Outline each blood parasite and name the species.
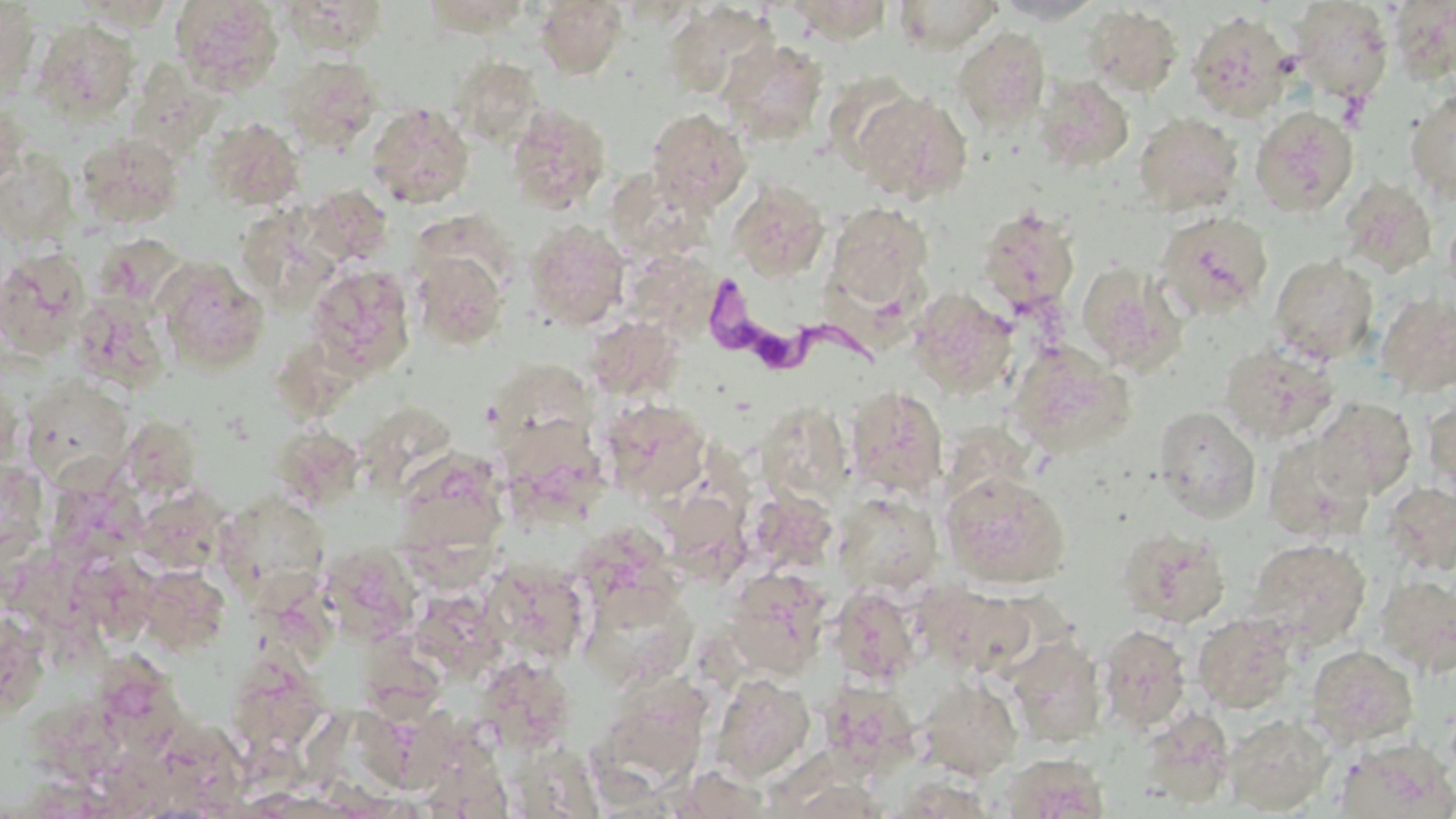
Approximate bounding boxes as [x1, y1, x2, y2] in pixels.
Trypanosoma brucei: [698, 274, 875, 373].
No Plasmodium falciparum, Plasmodium ovale, Plasmodium malariae, Plasmodium vivax, or Babesia divergens observed.

Uninfected red blood cell locations: [169, 0, 284, 94], [279, 0, 390, 57], [782, 0, 894, 43], [893, 0, 1003, 53], [991, 0, 1104, 24], [0, 1, 40, 96], [534, 1, 629, 80], [1290, 1, 1394, 103], [1389, 1, 1456, 84], [662, 4, 780, 99], [1081, 5, 1183, 96], [1186, 10, 1296, 120], [33, 18, 141, 122], [953, 27, 1051, 132], [717, 38, 829, 145], [280, 55, 382, 150], [450, 55, 543, 145], [1033, 74, 1133, 173], [1405, 88, 1456, 204], [852, 90, 971, 204], [0, 100, 26, 194], [367, 102, 475, 209], [505, 102, 612, 215], [1251, 106, 1358, 216], [645, 108, 752, 211], [1134, 111, 1244, 215], [204, 117, 306, 210], [75, 132, 185, 229], [1, 151, 77, 246], [1338, 177, 1438, 277], [727, 180, 829, 282], [623, 181, 725, 261], [728, 185, 934, 289], [826, 201, 935, 306], [977, 206, 1080, 314], [1155, 210, 1274, 321], [241, 211, 346, 297], [524, 219, 630, 330], [94, 233, 188, 311], [0, 247, 91, 357], [412, 249, 509, 351], [637, 251, 727, 340], [1268, 255, 1379, 364], [155, 257, 270, 375], [1077, 261, 1185, 374], [306, 266, 416, 377], [908, 288, 1018, 399], [1376, 292, 1456, 398], [72, 294, 170, 392], [584, 315, 685, 402], [1007, 340, 1135, 458], [1220, 341, 1341, 445], [497, 364, 603, 459], [17, 375, 146, 511], [845, 385, 948, 499], [1423, 395, 1456, 500], [1313, 397, 1418, 500], [599, 399, 712, 504], [757, 401, 853, 507], [1153, 405, 1261, 522], [365, 408, 460, 503], [271, 425, 364, 512], [1262, 432, 1374, 543], [492, 444, 597, 533], [54, 467, 155, 576], [940, 471, 1071, 589], [1382, 482, 1456, 575], [133, 486, 230, 575], [214, 489, 330, 605], [744, 489, 839, 575], [398, 490, 505, 595], [832, 491, 941, 596], [1116, 525, 1231, 628], [1247, 538, 1371, 648], [321, 543, 423, 644], [485, 562, 590, 663], [139, 564, 231, 655], [724, 568, 832, 679], [1375, 574, 1456, 676], [580, 578, 699, 689], [923, 583, 1035, 676], [831, 585, 924, 684], [422, 602, 521, 690], [0, 606, 47, 723], [1193, 612, 1300, 714], [1096, 624, 1191, 734], [1005, 635, 1107, 747], [102, 644, 196, 767], [1305, 644, 1419, 748], [226, 656, 328, 755], [480, 669, 574, 749], [710, 673, 815, 782], [917, 676, 1023, 779], [599, 683, 708, 766], [1138, 708, 1236, 807], [361, 711, 488, 793], [1224, 714, 1334, 814], [1335, 737, 1455, 819], [999, 753, 1109, 818]. Slide-level diagnosis: Trypanosoma brucei. Thin blood film. Single field of view. May-Grünwald-Giemsa-stained preparation. Captured at 1000x magnification. Optical microscopy. Image is 1456×819 pixels.